Classify this cell by malaria status.
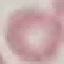

It is uninfected.

Giemsa-stained preparation. Photographed with a smartphone camera at the microscope eyepiece. Automatically extracted cell patch, resized to 64 × 64 pixels. Thin smear of blood.